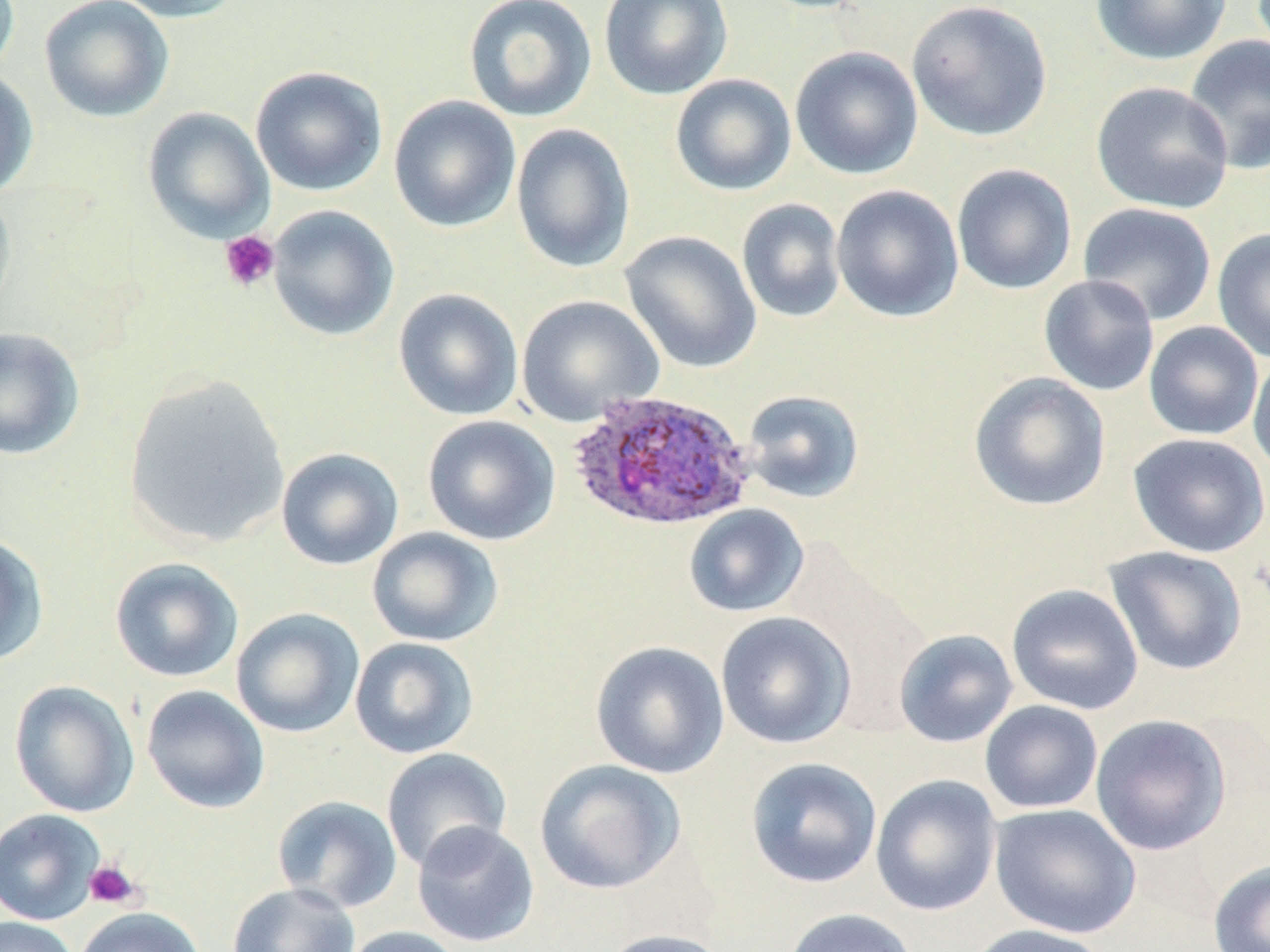

Summary:
  - Coordinate format: approximate bounding boxes as (x1,y1)-(x2,y2) corner pairs in pixels
  - Uninfected red blood cell locations: (0,0)-(20,78), (39,0)-(175,123), (108,0)-(248,23), (463,0)-(597,122), (598,0)-(733,100), (907,0)-(1053,142), (1089,0)-(1231,65), (1183,34)-(1269,175), (790,46)-(924,180), (250,66)-(388,196), (0,68)-(39,199), (670,73)-(797,196), (1091,81)-(1234,214), (388,95)-(521,233), (143,107)-(274,242), (510,123)-(636,273), (951,163)-(1077,295), (831,184)-(965,323), (0,187)-(16,324), (737,198)-(846,323), (1078,202)-(1217,326), (267,205)-(399,341), (1212,227)-(1270,363), (620,230)-(762,374), (1038,274)-(1159,396), (393,288)-(524,421), (517,294)-(664,427), (1144,321)-(1263,441), (0,326)-(85,460), (1248,351)-(1270,477), (968,371)-(1111,511), (123,374)-(291,549), (741,389)-(865,504), (422,415)-(561,546), (1127,432)-(1270,558), (276,447)-(403,570), (683,504)-(809,618), (366,527)-(504,648), (0,533)-(49,666), (1103,545)-(1248,676), (109,557)-(244,683), (1006,583)-(1144,715), (231,608)-(364,738), (715,611)-(856,749), (894,629)-(1018,748), (349,637)-(479,759), (590,641)-(729,779), (8,680)-(139,818), (141,685)-(270,814), (980,700)-(1103,814), (1089,714)-(1232,856), (381,747)-(512,873), (745,757)-(882,889), (534,759)-(686,894), (870,774)-(1002,917), (271,795)-(403,913), (989,803)-(1141,939), (0,808)-(105,926), (411,821)-(539,948), (1208,860)-(1270,952), (226,882)-(361,951), (74,906)-(205,952), (782,907)-(918,952), (0,916)-(79,952), (965,923)-(1112,952), (338,926)-(468,952), (598,928)-(732,952)
  - Platelet locations: (219,230)-(280,292), (84,859)-(142,909)
  - Plasmodium ovale-infected red blood cell locations: (566,390)-(756,531)
  - Slide-level diagnosis: Plasmodium ovale
  - Preparation: thin blood film
  - Field of view: one of a larger specimen
  - Magnification: 1000x
  - Stain: May-Grünwald-Giemsa
  - Modality: optical microscopy
  - Image size: 1270×952 pixels